Report the malaria status of this cell.
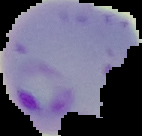

Parasitized.

Summary:
  - Image size: 142×136 pixels
  - Preparation: thin blood film
  - Image type: segmented cell region on a black background